State which parasite is depicted.
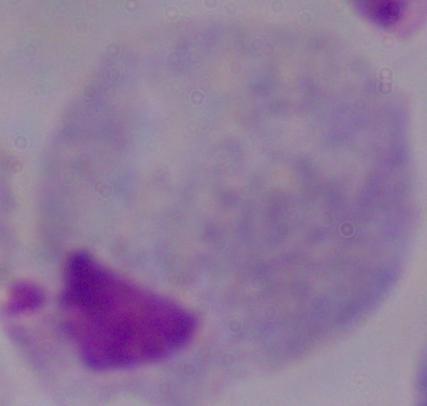

This is a trichomonad.

modality = photomicrograph
magnification = 1000x